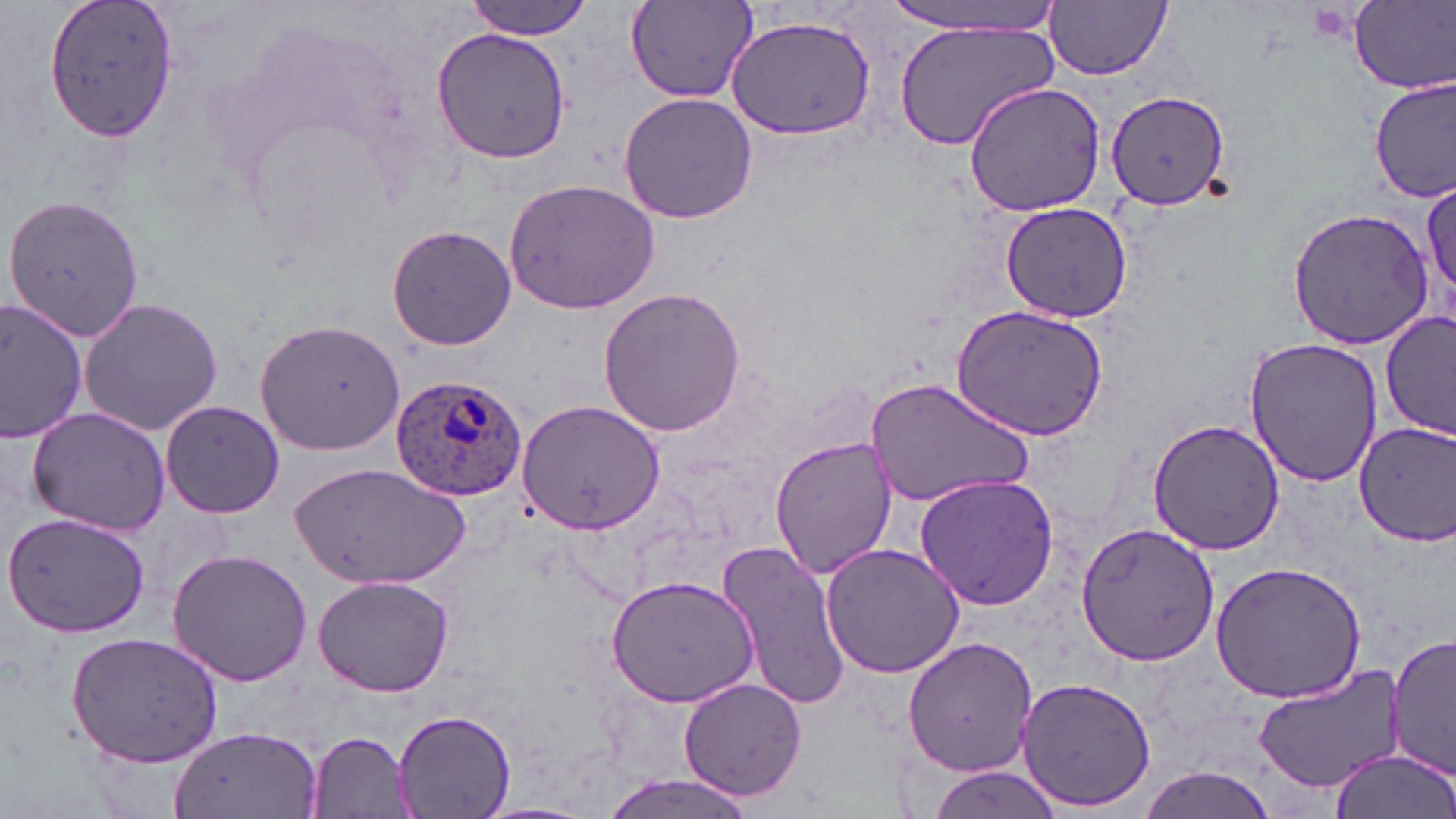 Approximate bounding boxes as (x1,y1)-(x2,y2) corner pairs in pixels. Uninfected red blood cell locations: (41,0)-(181,142), (463,0)-(592,39), (624,0)-(758,104), (885,0)-(1070,35), (1350,0)-(1456,91), (1046,1)-(1173,80), (724,15)-(876,139), (894,19)-(1058,152), (432,27)-(569,161), (1372,78)-(1455,203), (964,82)-(1107,216), (1105,88)-(1230,208), (618,93)-(756,225), (502,177)-(661,315), (1421,179)-(1455,306), (2,191)-(148,345), (998,202)-(1134,322), (1288,206)-(1437,348), (386,222)-(517,352), (597,286)-(745,439), (77,297)-(224,435), (0,299)-(86,443), (952,304)-(1110,440), (1381,308)-(1456,442), (255,316)-(406,455), (1246,337)-(1385,488), (866,376)-(1033,509), (516,396)-(665,538), (160,399)-(286,519), (27,406)-(173,535), (1146,419)-(1284,556), (1355,420)-(1456,547), (771,436)-(895,579), (293,464)-(470,590), (915,473)-(1062,611), (4,513)-(151,640), (1076,522)-(1218,667), (718,539)-(848,713), (820,542)-(964,680), (166,548)-(314,688), (1210,561)-(1368,703), (312,574)-(456,697), (607,574)-(760,706), (1388,630)-(1456,777), (63,631)-(228,768), (903,637)-(1039,775), (1248,661)-(1405,793), (1016,676)-(1155,812), (680,677)-(807,802), (393,707)-(517,818), (171,726)-(321,819), (307,732)-(418,819), (1328,749)-(1453,819), (925,763)-(1067,817), (1138,767)-(1279,819), (598,773)-(760,819), (471,803)-(601,819). Plasmodium ovale-infected red blood cell locations: (391,370)-(530,500). Slide-level diagnosis: Plasmodium ovale. May-Grünwald-Giemsa-stained preparation. Optical microscopy. Image is 1456×819 pixels. 1000x magnification. Single field of view. Thin blood smear.